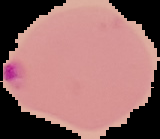
image size = 160×139 pixels
malaria status = parasitized
preparation = thin blood film
image type = cell region segmented out of the field of view; surrounding area masked to black